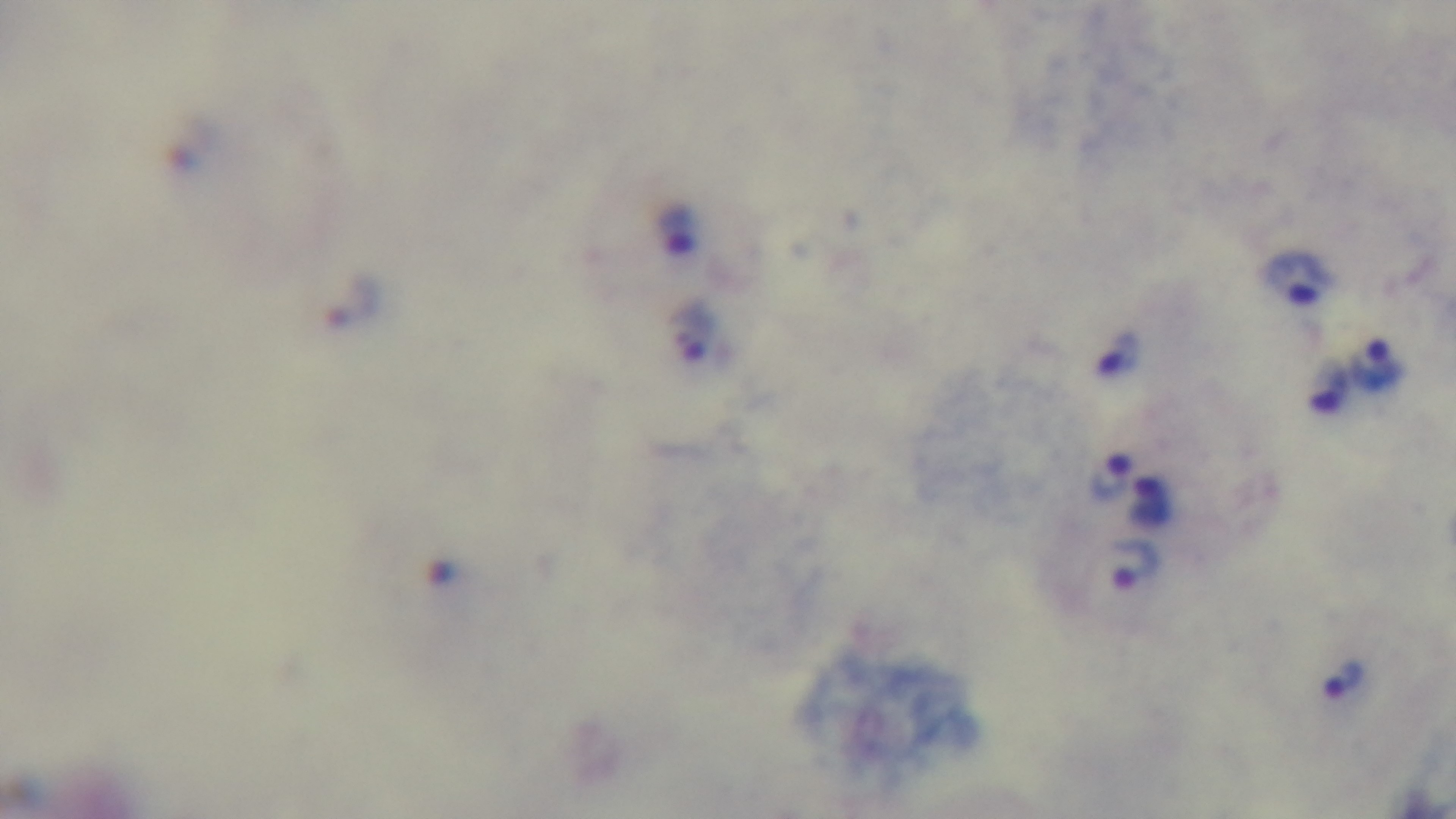

malaria status = infected
objective = 100x oil immersion
preparation = thick
field of view = one from the slide
stain = Giemsa
modality = light microscopy
capture = mounted 4K digital camera